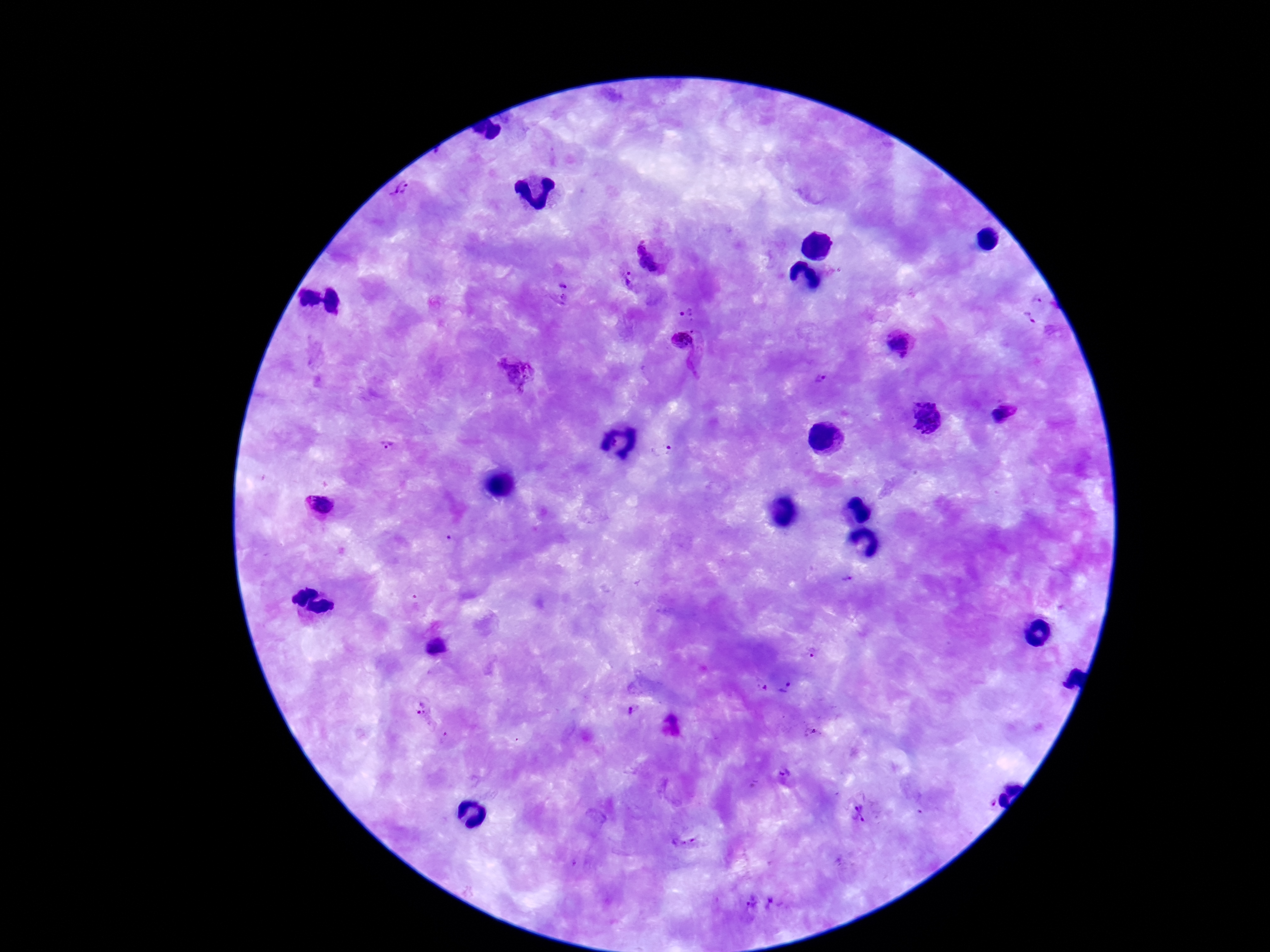
Approximate centers as (x, y) in pixels. Plasmodium parasite locations: (403, 194), (656, 252), (629, 273), (628, 282), (563, 284), (1037, 298), (563, 299), (681, 313), (1028, 322), (694, 331), (681, 340), (901, 343), (515, 371), (820, 379), (1006, 414), (928, 416), (390, 448), (660, 449), (320, 504), (851, 580), (435, 646), (814, 653), (762, 686), (785, 687), (422, 709), (632, 710), (812, 730), (785, 775), (859, 814). Patient malaria status: positive. Single field of view. Thick peripheral-blood smear. Image is 1270×952 pixels. Giemsa stain. 100x magnification. Smartphone photograph taken through the microscope eyepiece.